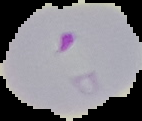

Image is 142×121 pixels. From a thin blood film. Malaria status: parasitized. Segmented cell region on a black background.